Identify the parasite.
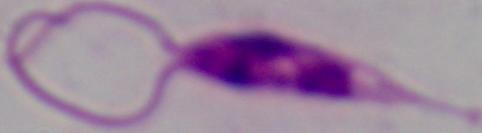

This is Leishmania.

1000x magnification. Micrograph.